State the preparation type.
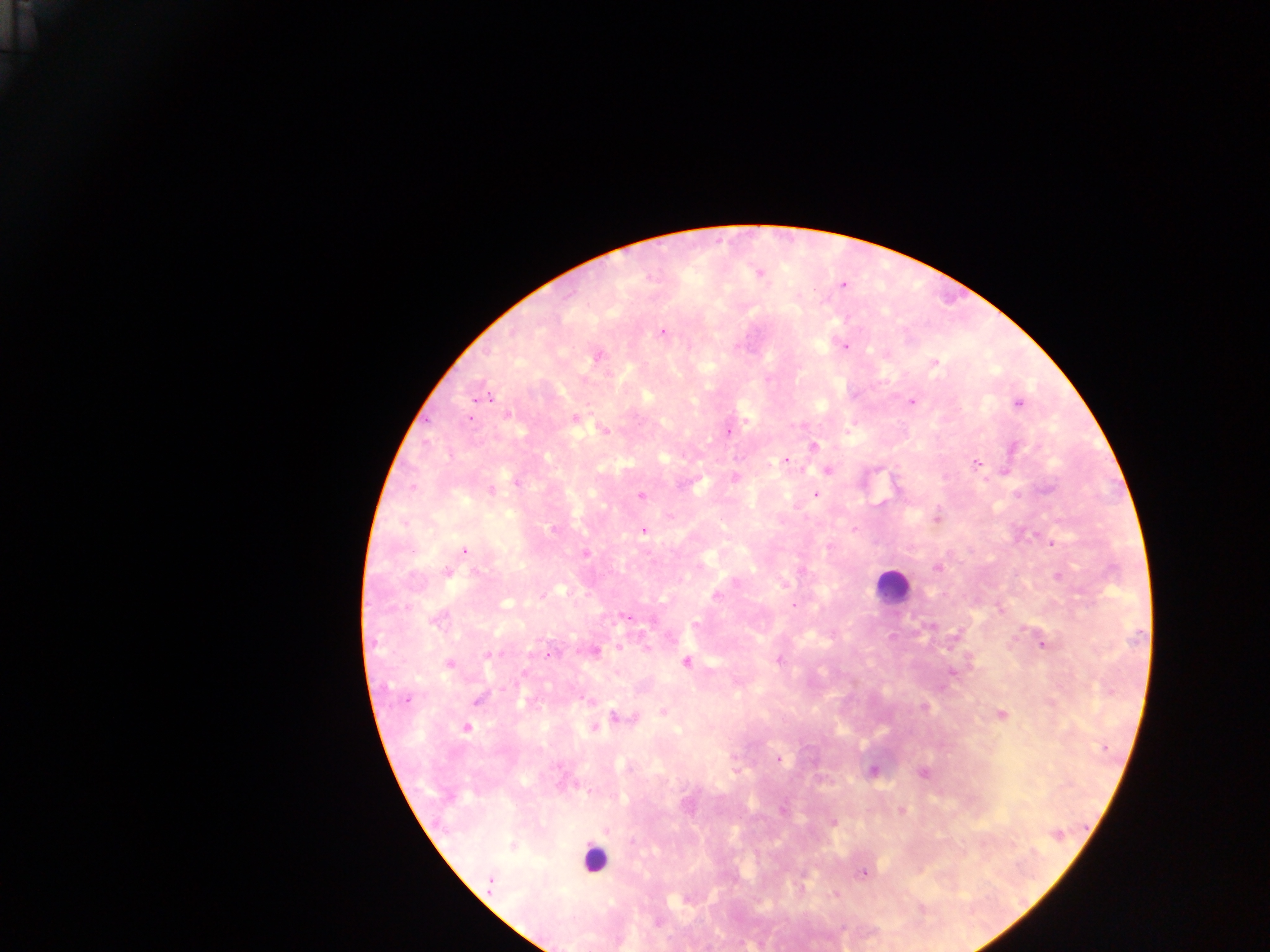
This is a thick smear.

Plasmodium parasite locations = approximate centers as x y in pixels: 759 273; 842 284; 661 332; 843 345; 595 357; 934 364; 482 395; 912 401; 1018 403; 507 415; 469 417; 575 418; 604 430; 727 430; 813 446; 1012 447; 785 460; 976 462; 827 470; 1004 471; 734 477; 516 481; 490 491; 641 494; 816 494; 937 517; 553 530; 643 530; 464 549; 584 553; 937 566; 447 572; 1059 576; 1000 609; 624 615; 438 618; 695 624; 1042 643; 647 646; 593 651; 489 654; 778 660; 686 662; 447 663; 951 672; 478 697; 406 700; 589 700; 924 706; 663 711; 1000 715; 621 717; 632 718; 594 727; 465 728; 778 759; 873 771; 923 772; 781 810; 901 811; 833 822; 606 829; 513 845; 862 873; 491 882; 834 894; 656 922
country = Ghana
capture = mobile-phone photograph through a microscope
image size = 1270×952 pixels
field of view = single
leukocyte locations = approximate centers as x y in pixels: 892 586; 593 859